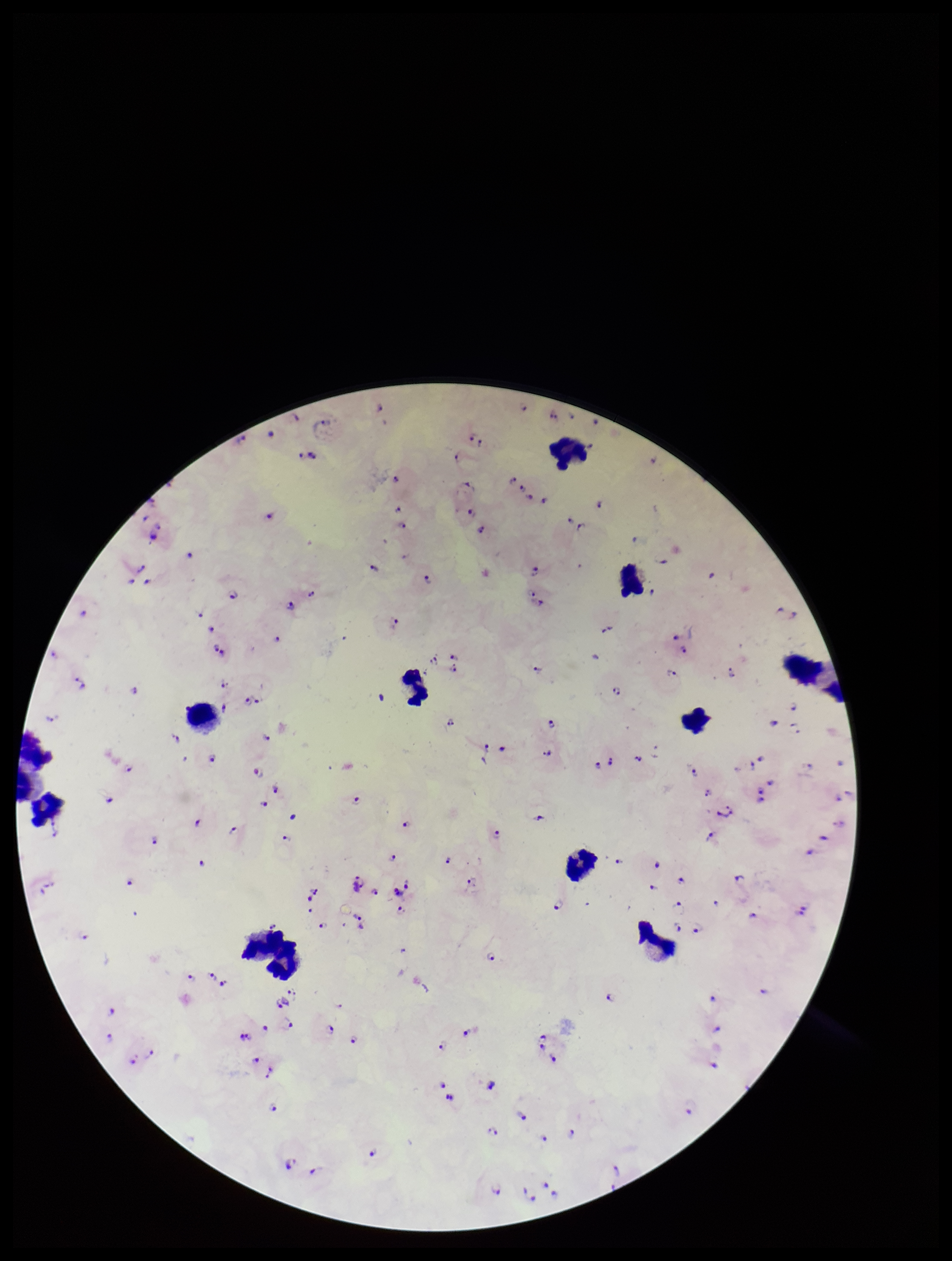
Summary:
  - Field of view: single
  - Image size: 952×1261 pixels
  - Plasmodium parasites: detected
  - Parasite count: 97
  - Patient malaria status: positive
  - Capture: smartphone photograph through the microscope eyepiece
  - Species reported for this patient: Plasmodium falciparum
  - Preparation: thick smear
  - Leukocyte count: 11
  - Stain: Giemsa